Give the position of every leukocyte visible.
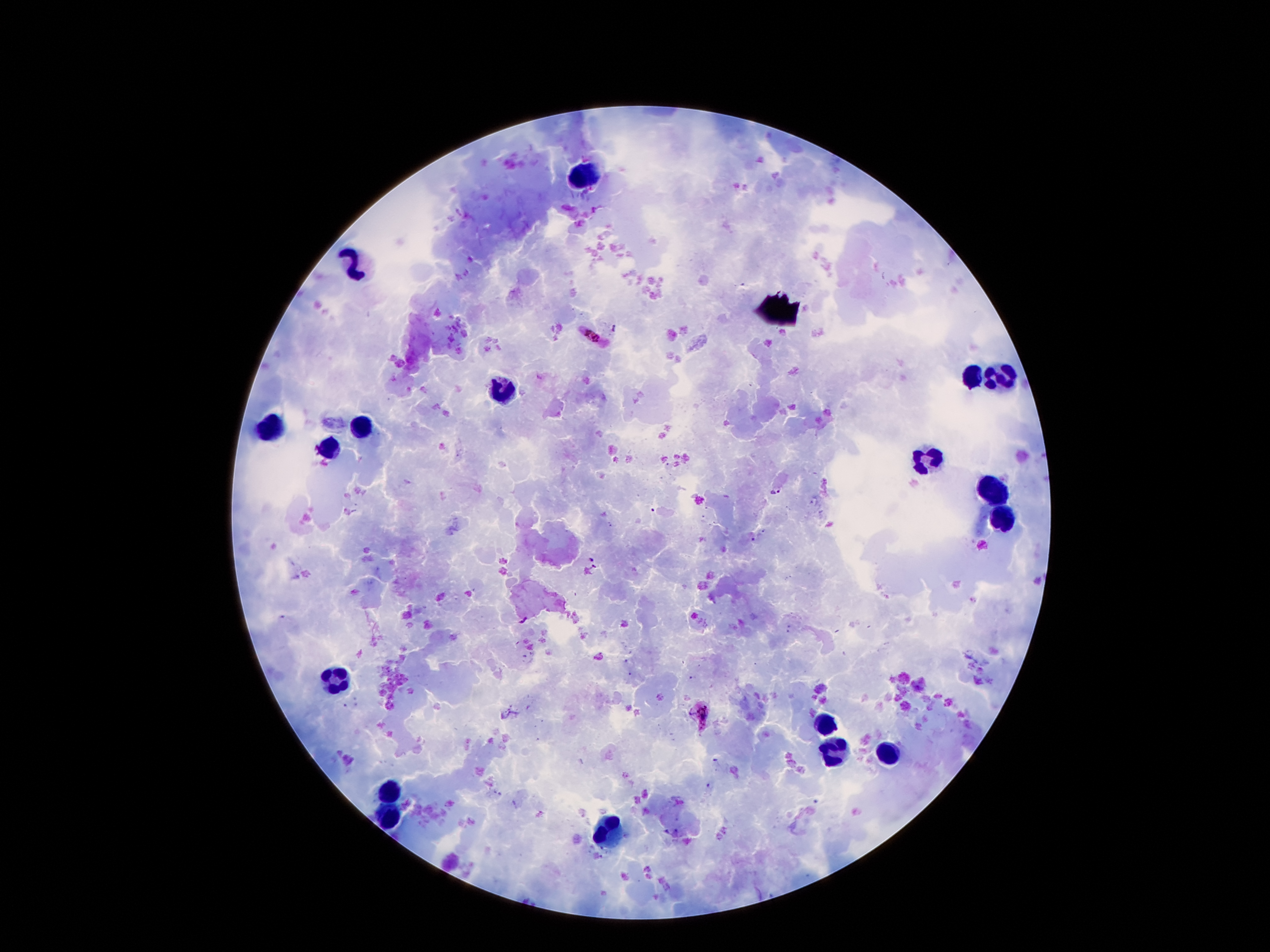
Approximate centers as {x, y} in pixels.
Leukocytes: {581, 173}, {352, 262}, {972, 377}, {996, 377}, {502, 390}, {364, 426}, {268, 430}, {327, 452}, {926, 461}, {990, 488}, {1004, 516}, {334, 679}, {821, 725}, {833, 753}, {888, 755}, {393, 790}, {390, 819}, {610, 832}.

Summary:
  - Plasmodium parasite locations: {616, 327}, {593, 337}, {776, 491}, {594, 564}, {524, 619}, {704, 713}
  - Capture: smartphone camera through the microscope eyepiece
  - Patient malaria status: positive for Plasmodium falciparum
  - Magnification: 100x
  - Field of view: single
  - Image size: 1270×952 pixels
  - Stain: Giemsa
  - Preparation: thick peripheral-blood smear